State which cell type is depicted.
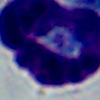

A leukocyte.

magnification = 1000x
modality = photomicrograph